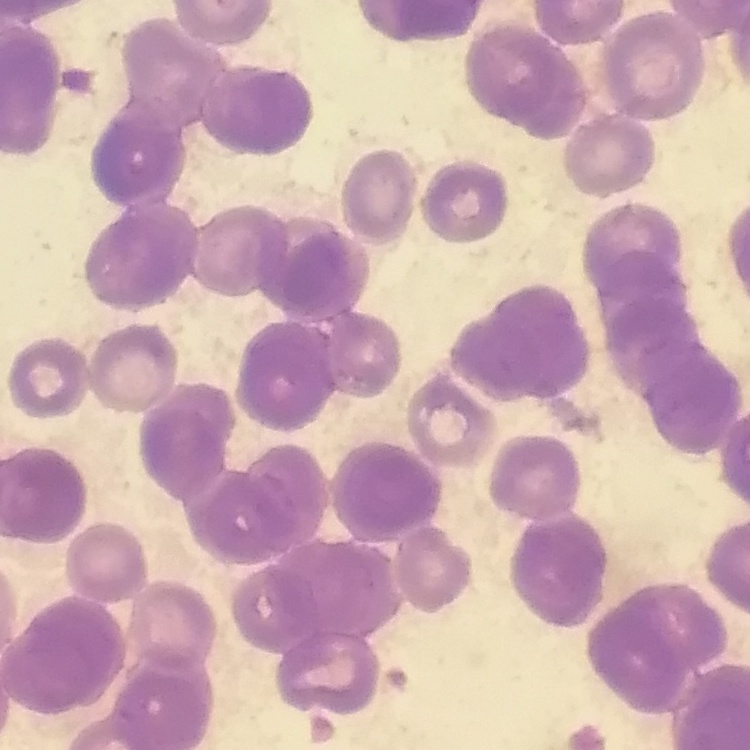

Summary:
  - Erythrocyte morphology: rouleaux formation
  - Preparation: thin blood film
  - Image type: square crop of a larger photomicrograph
  - Stain: Field's or Giemsa